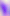

400x magnification. Photomicrograph. Toxoplasma gondii is shown.